Name the parasite shown.
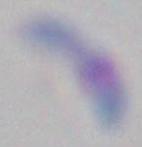

Toxoplasma gondii.

Summary:
  - Magnification: 1000x
  - Modality: micrograph